State which parasite is depicted.
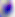
Toxoplasma gondii.

magnification = 400x
modality = micrograph